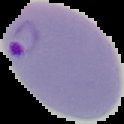

Summary:
  - Result: Plasmodium parasites detected
  - Image size: 124×124 pixels
  - Preparation: thin blood smear
  - Image type: segmented cell region with the area outside set to black